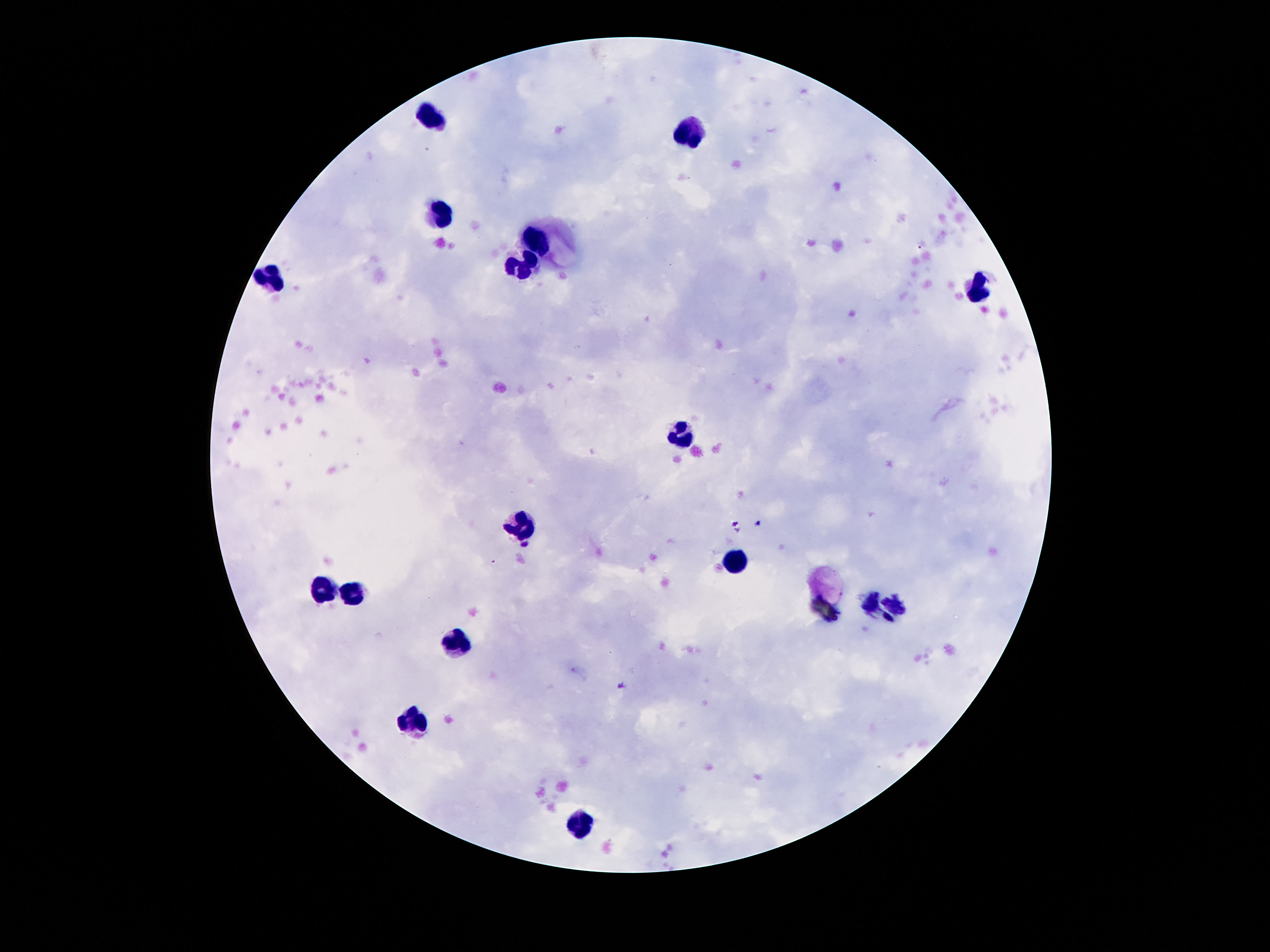

Approximate object centers, in pixels from the top-left corner. Leukocyte locations: (x=431, y=115), (x=687, y=130), (x=435, y=213), (x=536, y=242), (x=526, y=261), (x=271, y=276), (x=974, y=289), (x=683, y=434), (x=517, y=528), (x=737, y=563), (x=321, y=589), (x=356, y=594), (x=455, y=640), (x=416, y=718), (x=580, y=824). Thick peripheral-blood smear. 100x magnification. One field from this slide. Smartphone photograph taken through the microscope eyepiece. Giemsa stain. Patient malaria status: not infected. Image is 1270×952 pixels.